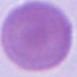

magnification = 1000x
modality = micrograph
identification = red blood cell